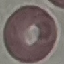

result = no malaria parasites detected
capture = smartphone camera at the microscope eyepiece
stain = Giemsa
preparation = thin smear
image type = cell patch, automatically extracted from a larger field of view and resized to 64 × 64 pixels